Describe the morphology of the red blood cells.
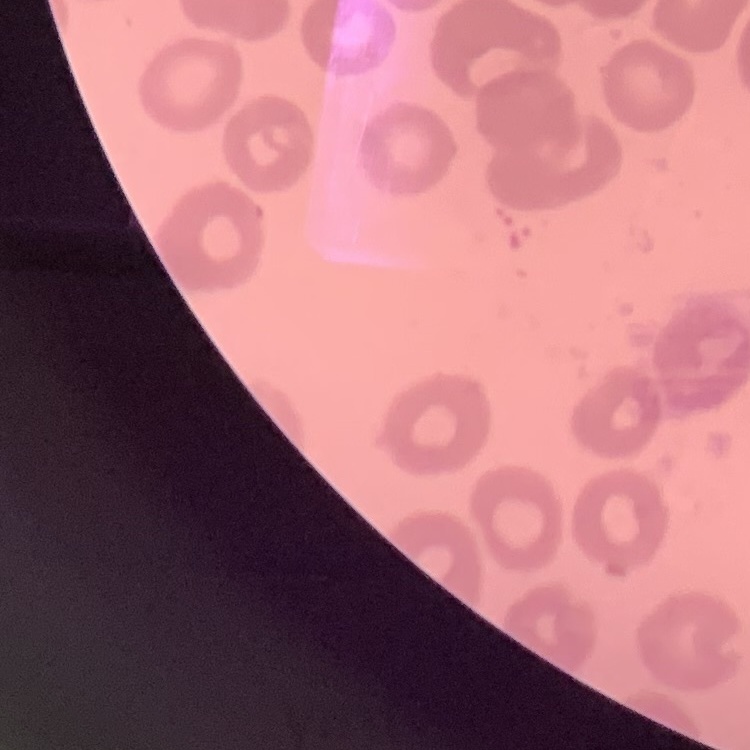

They show no rouleaux formation.

Thin peripheral smear. One tile cut from a larger photomicrograph. Stained with either Field's or Giemsa.